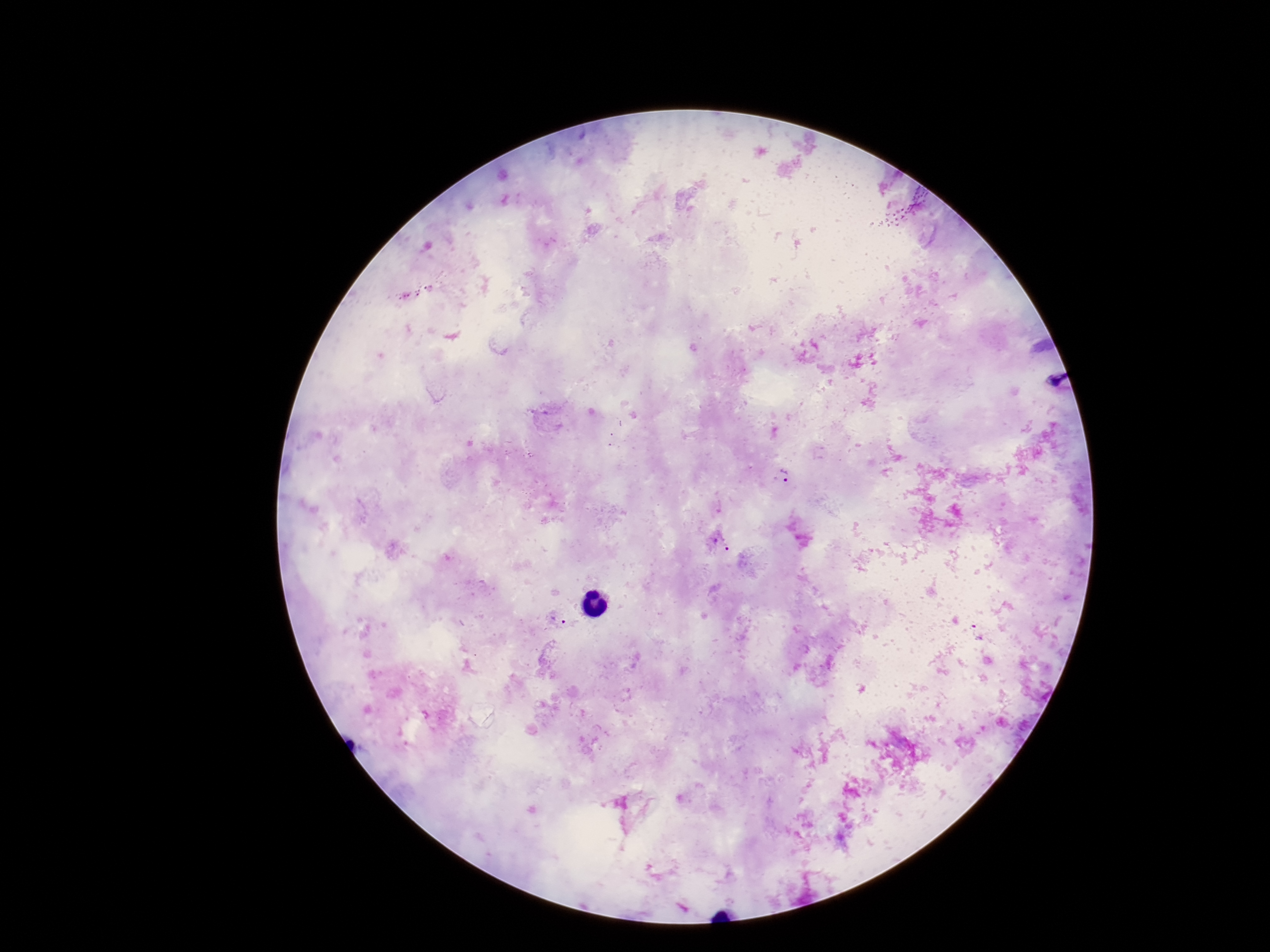

field of view = one from this slide
Plasmodium parasite locations = approximate centers as [x, y] in pixels: [781, 475], [720, 544], [559, 619]
patient malaria status = positive
image size = 1270×952 pixels
magnification = 100x
stain = Giemsa
preparation = thick peripheral-blood smear
capture = smartphone camera through the microscope eyepiece